Give a bounding box for every parasitised red blood cell, every trophozoite, every gametocyte, every leukocyte, and every artifact (platelet-like body, stain precipitate, or debris).
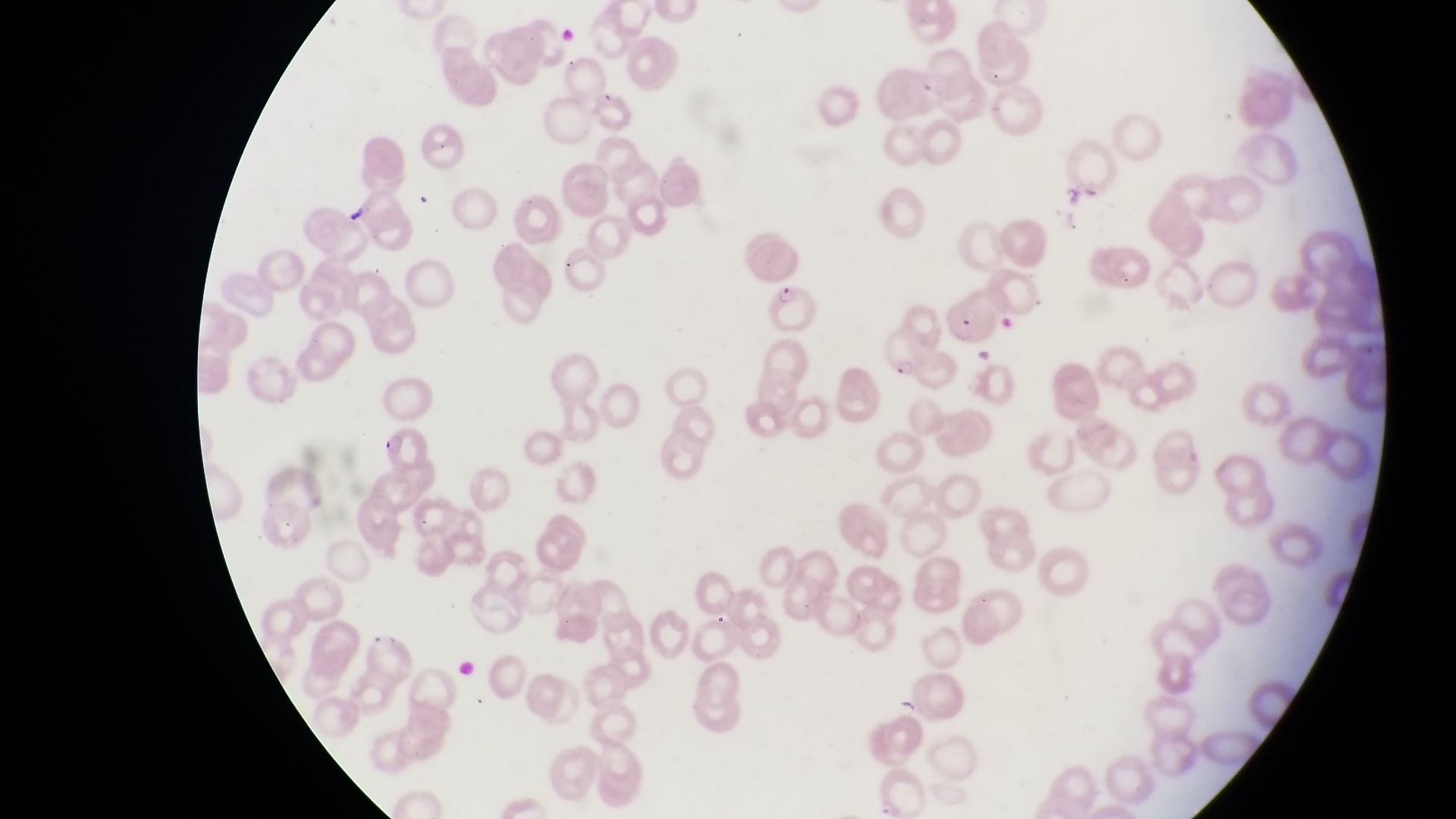
Approximate bounding boxes as (left, top, right, bottom) in pixels.
Parasitised red blood cells: (764, 277, 820, 337), (944, 298, 999, 348), (880, 325, 926, 381), (373, 423, 432, 473).
No leukocytes observed.

country = Uganda
image size = 1456×819 pixels
capture = smartphone photograph through the eyepiece of an Olympus CX-23 microscope
preparation = thin blood smear
magnification = 1000x
field of view = single